Name the blood parasite species.
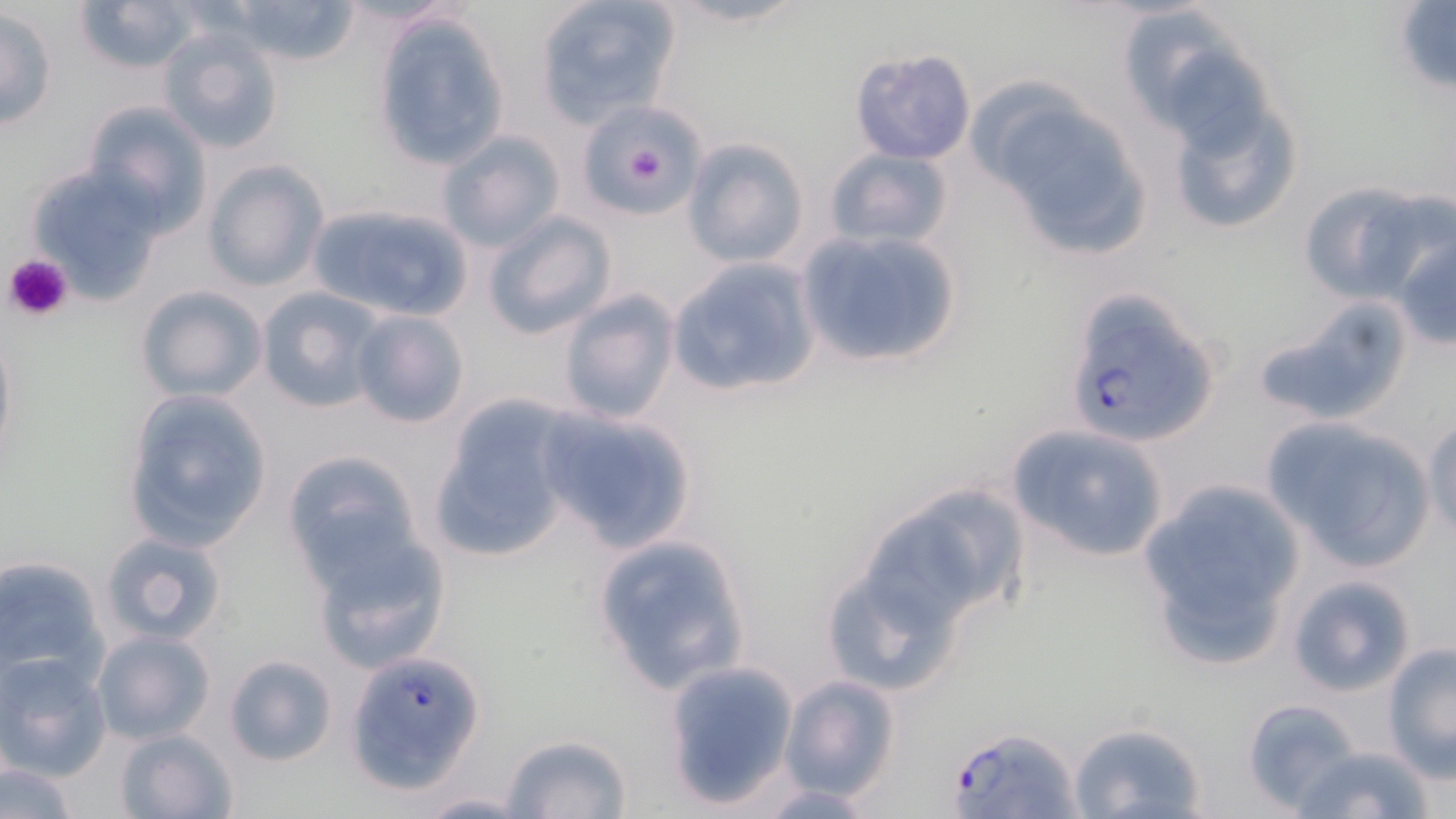

Plasmodium falciparum.

preparation = thin blood smear
platelet locations = approximate bounding boxes as named x1/y1/x2/y2 corners in pixels: (x1=612, y1=128, x2=676, y2=198), (x1=4, y1=254, x2=73, y2=323)
uninfected red blood cell locations = approximate bounding boxes as named x1/y1/x2/y2 corners in pixels: (x1=71, y1=0, x2=207, y2=76), (x1=533, y1=0, x2=682, y2=129), (x1=221, y1=1, x2=366, y2=70), (x1=1392, y1=3, x2=1456, y2=94), (x1=2, y1=6, x2=58, y2=130), (x1=369, y1=11, x2=510, y2=171), (x1=157, y1=27, x2=286, y2=155), (x1=397, y1=44, x2=535, y2=232), (x1=848, y1=47, x2=976, y2=166), (x1=1147, y1=51, x2=1307, y2=239), (x1=979, y1=92, x2=1158, y2=264), (x1=79, y1=99, x2=213, y2=232), (x1=579, y1=102, x2=700, y2=218), (x1=436, y1=130, x2=565, y2=253), (x1=683, y1=136, x2=810, y2=270), (x1=824, y1=147, x2=955, y2=249), (x1=203, y1=160, x2=329, y2=292), (x1=27, y1=164, x2=171, y2=304), (x1=1297, y1=180, x2=1447, y2=307), (x1=314, y1=204, x2=476, y2=316), (x1=482, y1=211, x2=618, y2=340), (x1=1391, y1=227, x2=1456, y2=350), (x1=796, y1=229, x2=963, y2=370), (x1=663, y1=257, x2=822, y2=400), (x1=136, y1=285, x2=268, y2=404), (x1=255, y1=288, x2=386, y2=415), (x1=555, y1=290, x2=680, y2=426), (x1=1252, y1=297, x2=1416, y2=426), (x1=350, y1=311, x2=469, y2=429), (x1=0, y1=322, x2=17, y2=474), (x1=119, y1=389, x2=274, y2=553), (x1=430, y1=398, x2=577, y2=563), (x1=531, y1=406, x2=698, y2=550), (x1=1261, y1=416, x2=1437, y2=569), (x1=1423, y1=420, x2=1455, y2=541), (x1=1005, y1=423, x2=1169, y2=563), (x1=281, y1=451, x2=425, y2=583), (x1=1134, y1=479, x2=1307, y2=668), (x1=914, y1=483, x2=1031, y2=606), (x1=865, y1=505, x2=981, y2=622), (x1=308, y1=529, x2=450, y2=671), (x1=99, y1=531, x2=229, y2=647), (x1=589, y1=532, x2=754, y2=697), (x1=0, y1=555, x2=108, y2=690), (x1=1285, y1=574, x2=1416, y2=697), (x1=841, y1=588, x2=957, y2=684), (x1=91, y1=630, x2=215, y2=745), (x1=1382, y1=643, x2=1456, y2=777), (x1=223, y1=653, x2=339, y2=767), (x1=0, y1=654, x2=110, y2=779), (x1=660, y1=662, x2=799, y2=810), (x1=778, y1=674, x2=903, y2=803), (x1=1242, y1=698, x2=1366, y2=814), (x1=1066, y1=721, x2=1209, y2=818), (x1=113, y1=728, x2=237, y2=819), (x1=500, y1=733, x2=632, y2=818), (x1=1292, y1=743, x2=1436, y2=818), (x1=0, y1=760, x2=83, y2=818), (x1=752, y1=782, x2=887, y2=816), (x1=412, y1=791, x2=533, y2=817)
image size = 1456×819 pixels
Plasmodium falciparum-infected red blood cell locations = approximate bounding boxes as named x1/y1/x2/y2 corners in pixels: (x1=1064, y1=288, x2=1218, y2=450), (x1=346, y1=651, x2=485, y2=795), (x1=944, y1=725, x2=1082, y2=819)
modality = light microscopy
field of view = single
stain = May-Grünwald-Giemsa
magnification = 1000x